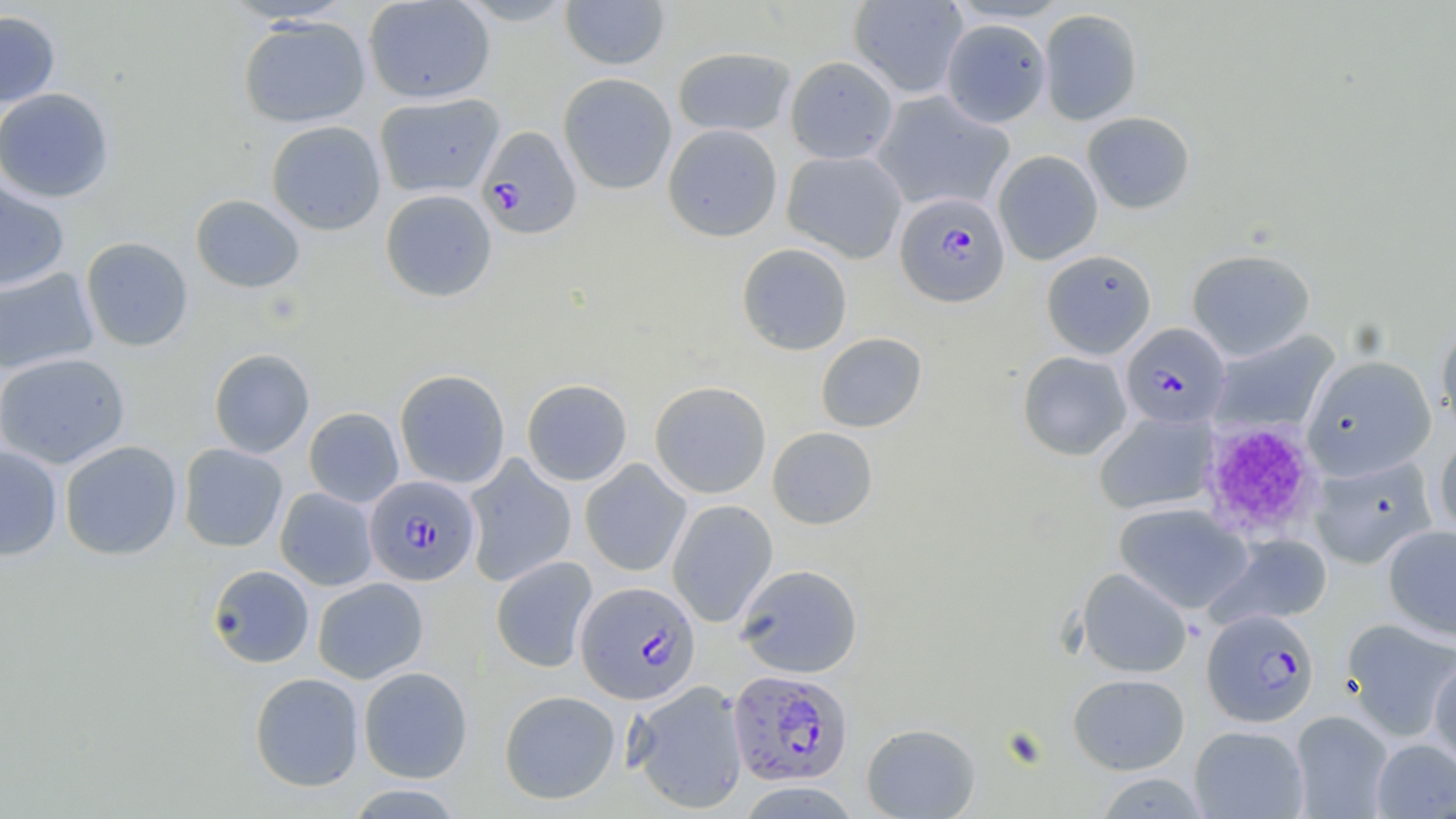 Approximate bounding boxes as [x1, y1, x2, y2] in pixels. Uninfected red blood cell locations: [362, 0, 496, 104], [454, 0, 578, 26], [560, 1, 670, 70], [848, 1, 968, 98], [1039, 8, 1142, 125], [0, 10, 61, 108], [238, 16, 371, 128], [941, 19, 1051, 127], [672, 46, 796, 137], [785, 56, 899, 164], [557, 73, 677, 195], [0, 87, 115, 203], [872, 91, 1014, 212], [374, 92, 504, 198], [1082, 111, 1195, 214], [266, 120, 386, 235], [662, 123, 782, 242], [782, 149, 907, 263], [992, 150, 1103, 265], [0, 179, 70, 291], [380, 188, 498, 303], [191, 194, 305, 293], [80, 236, 194, 352], [736, 243, 853, 356], [1186, 248, 1316, 360], [1041, 249, 1156, 359], [0, 268, 99, 375], [1436, 322, 1456, 436], [1211, 330, 1339, 435], [815, 332, 927, 433], [209, 348, 314, 458], [1017, 351, 1132, 461], [0, 352, 131, 469], [1302, 355, 1436, 479], [394, 369, 511, 489], [521, 378, 633, 486], [649, 381, 771, 499], [303, 407, 404, 507], [1094, 410, 1217, 514], [767, 427, 878, 529], [1434, 433, 1456, 543], [59, 440, 182, 560], [178, 443, 288, 552], [0, 445, 63, 560], [463, 455, 577, 587], [1310, 456, 1436, 569], [580, 460, 692, 577], [275, 487, 378, 590], [667, 499, 778, 627], [1114, 503, 1252, 614], [1383, 525, 1456, 640], [1210, 533, 1333, 628], [490, 555, 598, 673], [206, 564, 315, 668], [735, 564, 863, 678], [1077, 568, 1192, 678], [312, 577, 428, 683], [1341, 618, 1456, 740], [1428, 657, 1456, 770], [358, 666, 473, 783], [249, 672, 364, 792], [1068, 673, 1190, 775], [627, 680, 749, 814], [499, 689, 620, 804], [1290, 710, 1394, 818], [861, 722, 981, 818], [1189, 725, 1309, 818], [1371, 738, 1456, 818], [1095, 773, 1208, 818], [340, 783, 467, 818]. Plasmodium falciparum-infected red blood cell locations: [476, 125, 582, 239], [896, 192, 1010, 306], [1120, 323, 1230, 428], [364, 475, 481, 586], [575, 581, 701, 704], [1201, 609, 1321, 727], [727, 669, 852, 787]. Platelet locations: [1198, 421, 1320, 540]. Slide-level diagnosis: Plasmodium falciparum. May-Grünwald-Giemsa stain. Thin blood smear. Optical microscopy. Image is 1456×819 pixels. Single field of view. 1000x magnification.